State which parasite is depicted.
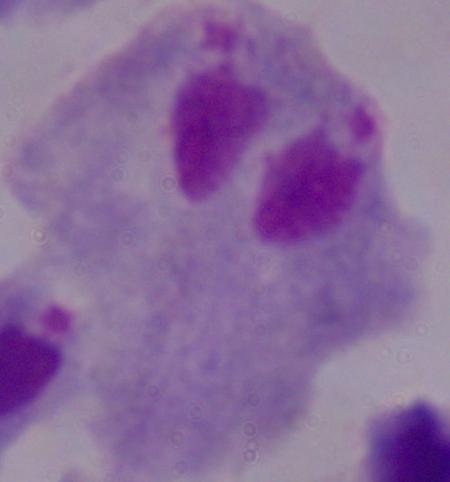

This is a trichomonad.

magnification = 1000x
modality = photomicrograph